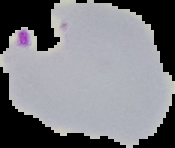

Summary:
  - Image size: 175×148 pixels
  - Malaria status: parasitized
  - Preparation: thin blood film
  - Image type: segmented cell region on a black background